Report the malaria status of this cell.
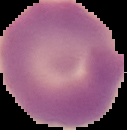

Parasitized.

Image is 127×130 pixels. From a thin blood smear. Cell region segmented out of the field of view; the surrounding area is masked to black.